Give the extent of all Babesia divergens-infected red blood cells.
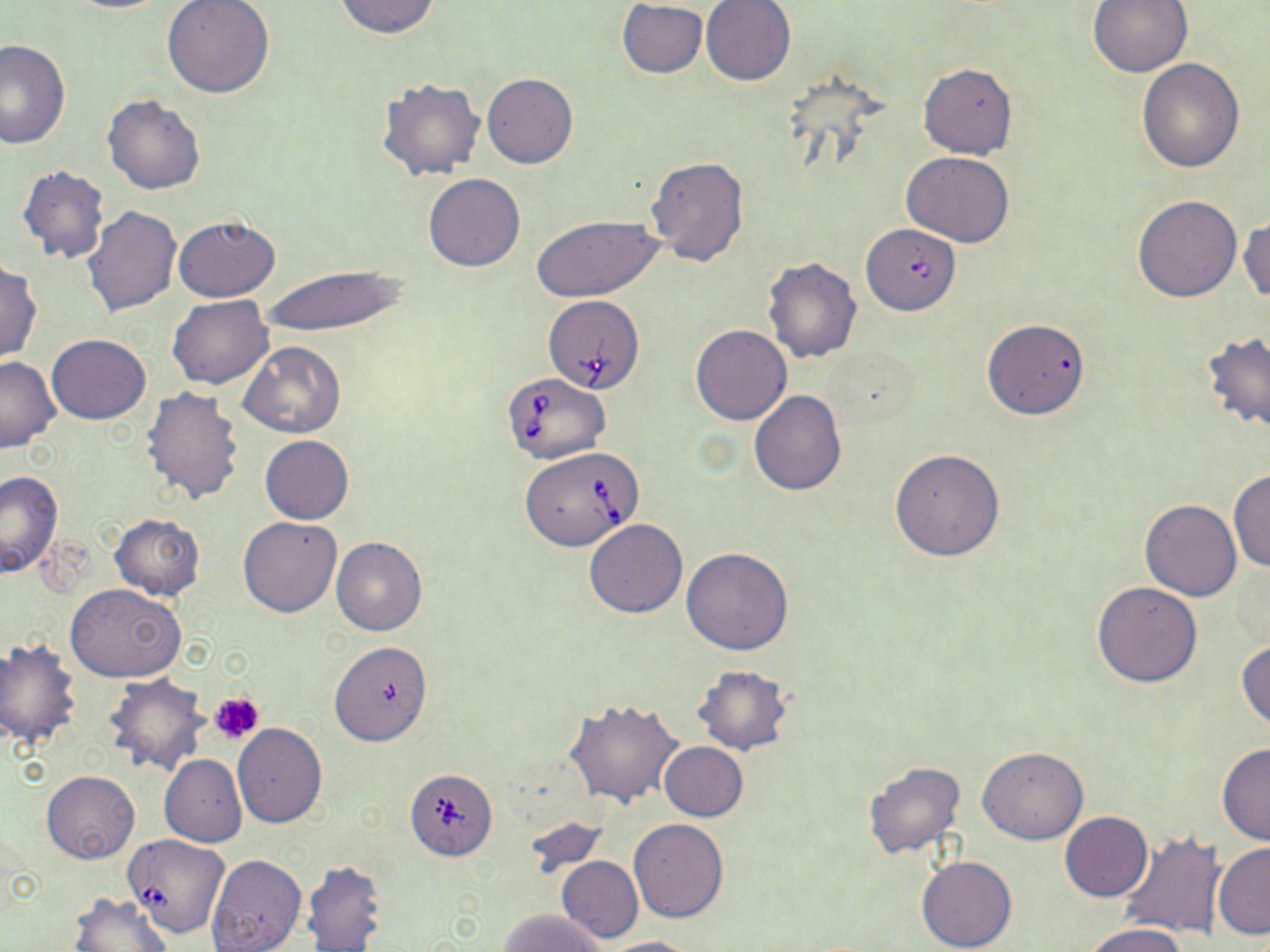

Approximate bounding boxes as named x1/y1/x2/y2 corners in pixels.
Babesia divergens-infected red blood cells: (x1=857, y1=220, x2=962, y2=318), (x1=544, y1=295, x2=646, y2=394), (x1=503, y1=373, x2=610, y2=465), (x1=519, y1=448, x2=643, y2=551), (x1=408, y1=769, x2=498, y2=865), (x1=124, y1=833, x2=232, y2=938).

Summary:
  - Uninfected red blood cell locations: (x1=61, y1=0, x2=177, y2=13), (x1=330, y1=0, x2=443, y2=39), (x1=701, y1=0, x2=796, y2=85), (x1=1087, y1=0, x2=1192, y2=78), (x1=162, y1=1, x2=276, y2=101), (x1=616, y1=1, x2=708, y2=78), (x1=0, y1=39, x2=70, y2=150), (x1=1136, y1=58, x2=1246, y2=173), (x1=918, y1=62, x2=1017, y2=159), (x1=482, y1=73, x2=577, y2=170), (x1=377, y1=77, x2=485, y2=180), (x1=102, y1=94, x2=205, y2=196), (x1=902, y1=151, x2=1015, y2=247), (x1=646, y1=156, x2=748, y2=269), (x1=17, y1=166, x2=110, y2=266), (x1=422, y1=173, x2=525, y2=272), (x1=1131, y1=195, x2=1241, y2=302), (x1=83, y1=205, x2=182, y2=319), (x1=531, y1=213, x2=663, y2=301), (x1=172, y1=214, x2=282, y2=302), (x1=1239, y1=214, x2=1269, y2=306), (x1=763, y1=257, x2=862, y2=363), (x1=0, y1=258, x2=43, y2=363), (x1=261, y1=265, x2=406, y2=337), (x1=167, y1=296, x2=272, y2=390), (x1=981, y1=319, x2=1090, y2=419), (x1=691, y1=325, x2=791, y2=424), (x1=1200, y1=331, x2=1270, y2=437), (x1=47, y1=334, x2=151, y2=424), (x1=239, y1=341, x2=345, y2=439), (x1=825, y1=344, x2=921, y2=431), (x1=0, y1=354, x2=60, y2=452), (x1=139, y1=386, x2=245, y2=506), (x1=749, y1=391, x2=847, y2=495), (x1=260, y1=435, x2=353, y2=525), (x1=890, y1=448, x2=1005, y2=561), (x1=1229, y1=468, x2=1269, y2=572), (x1=0, y1=471, x2=63, y2=578), (x1=1139, y1=499, x2=1242, y2=601), (x1=110, y1=513, x2=205, y2=600), (x1=237, y1=516, x2=343, y2=617), (x1=584, y1=519, x2=686, y2=618), (x1=330, y1=536, x2=426, y2=636), (x1=681, y1=546, x2=794, y2=654), (x1=1092, y1=581, x2=1202, y2=687), (x1=65, y1=583, x2=185, y2=682), (x1=0, y1=638, x2=82, y2=752), (x1=1236, y1=638, x2=1270, y2=731), (x1=329, y1=641, x2=433, y2=746), (x1=690, y1=664, x2=793, y2=755), (x1=102, y1=674, x2=208, y2=776), (x1=564, y1=697, x2=685, y2=808), (x1=232, y1=722, x2=327, y2=827), (x1=659, y1=742, x2=748, y2=821), (x1=1216, y1=743, x2=1270, y2=845), (x1=978, y1=746, x2=1088, y2=844), (x1=159, y1=754, x2=246, y2=846), (x1=863, y1=761, x2=967, y2=861), (x1=41, y1=770, x2=140, y2=864), (x1=1060, y1=812, x2=1152, y2=902), (x1=628, y1=818, x2=729, y2=923), (x1=1116, y1=829, x2=1225, y2=936), (x1=1213, y1=842, x2=1270, y2=939), (x1=205, y1=854, x2=307, y2=952), (x1=916, y1=856, x2=1017, y2=952), (x1=556, y1=857, x2=643, y2=943), (x1=304, y1=859, x2=387, y2=952), (x1=68, y1=892, x2=173, y2=952), (x1=500, y1=907, x2=608, y2=952), (x1=1082, y1=924, x2=1190, y2=952), (x1=596, y1=936, x2=697, y2=952)
  - Platelet locations: (x1=210, y1=692, x2=264, y2=744)
  - Slide-level diagnosis: Babesia divergens
  - Field of view: single
  - Image size: 1270×952 pixels
  - Stain: May-Grünwald-Giemsa
  - Preparation: thin blood smear
  - Modality: optical microscopy
  - Magnification: 1000x